Report the malaria status of this cell.
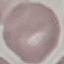
Uninfected.

preparation = thin blood smear
capture = smartphone camera at the microscope eyepiece
stain = Giemsa
image type = automatically extracted cell patch, resized to 64 × 64 pixels